Report the malaria status of this cell.
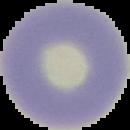

It is uninfected.

Summary:
  - Preparation: thin blood smear
  - Image size: 130×130 pixels
  - Image type: segmented cell region on a black background